Assess the morphology of the erythrocytes.
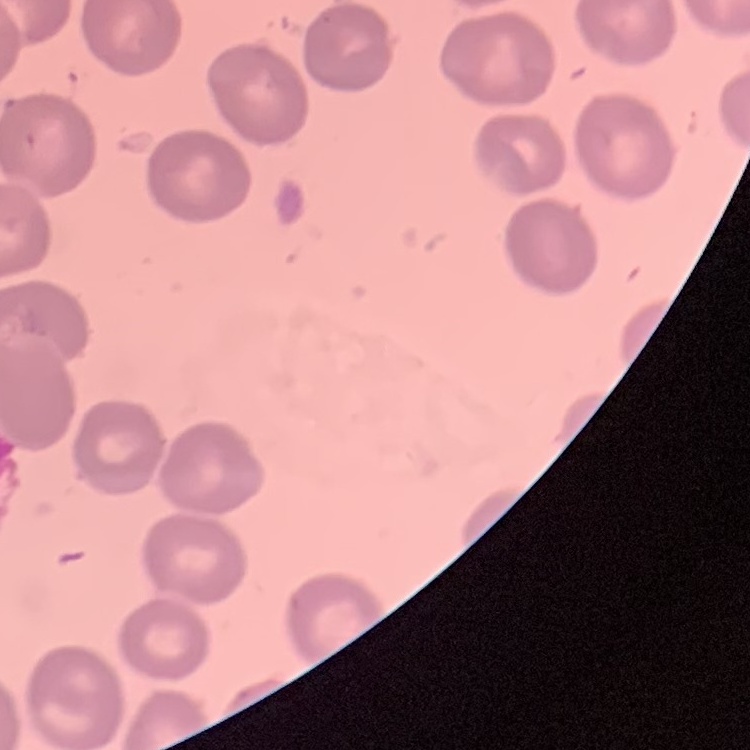
No rouleaux formation.

image type = square crop of a larger photomicrograph
stain = Field's or Giemsa
preparation = thin blood smear